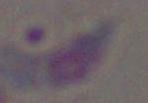 1000x magnification. Toxoplasma gondii is seen. Photomicrograph.